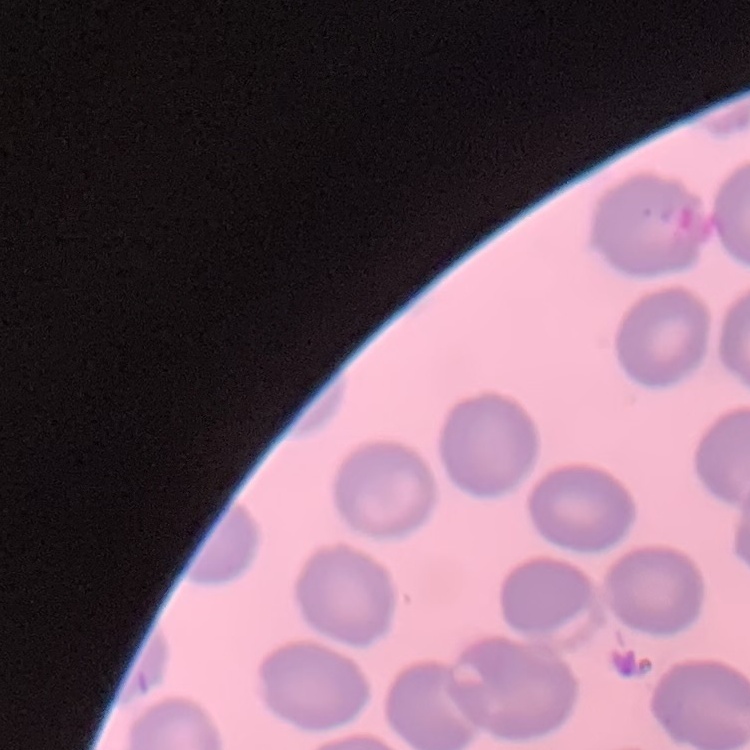

erythrocyte morphology = no rouleaux formation
preparation = thin blood film
image type = one tile cut from a larger photomicrograph
stain = Field's or Giemsa